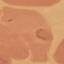

result = malaria parasites detected
image type = automatically extracted cell patch, resized to 64 × 64 pixels
preparation = thin blood smear
capture = smartphone through the microscope eyepiece
stain = Giemsa